Outline each uninfected red blood cell.
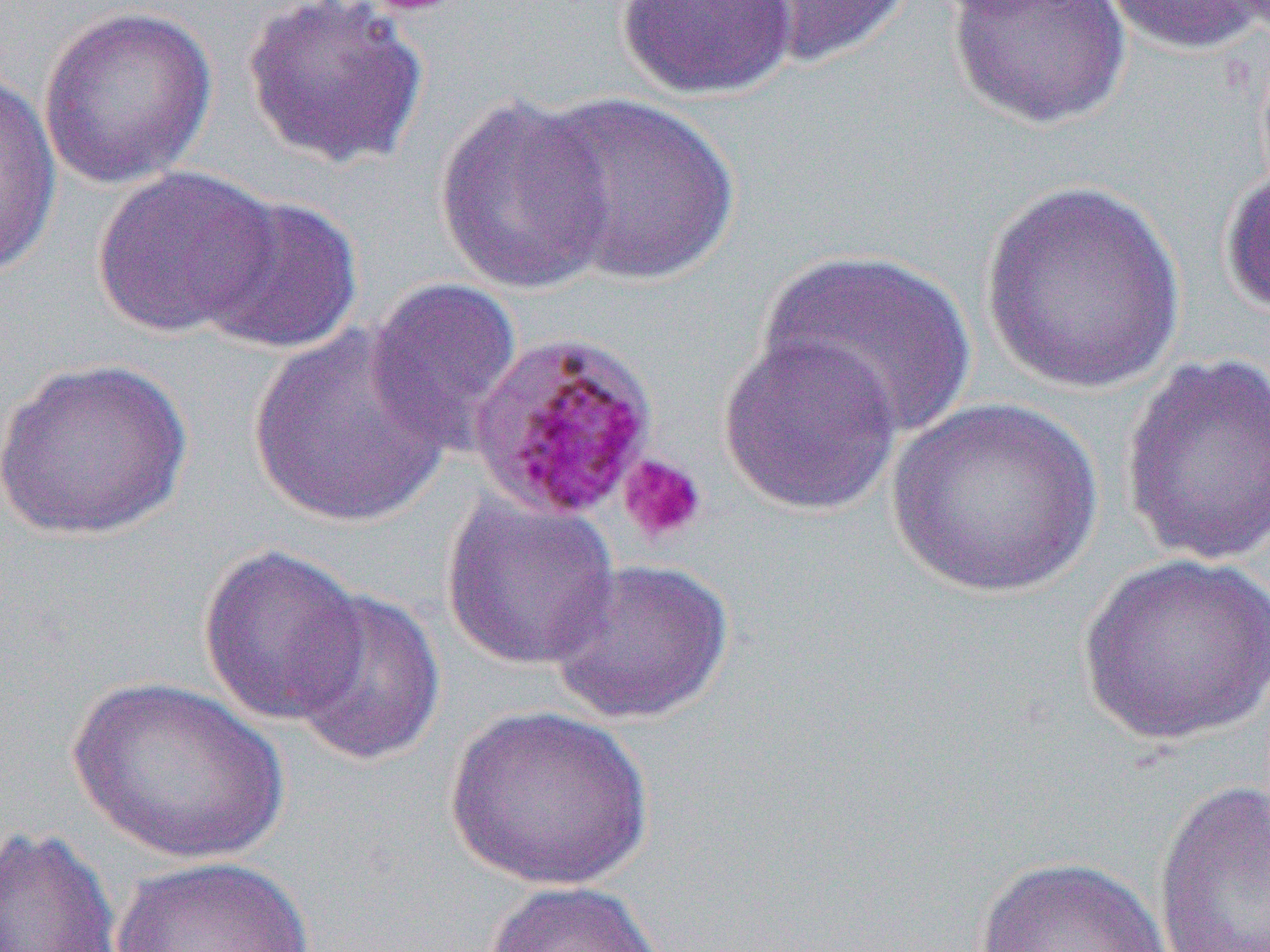

Approximate bounding boxes as (x1,y1)-(x2,y2) corner pairs in pixels.
Uninfected red blood cells: (240,0)-(430,172), (616,0)-(798,100), (734,0)-(916,70), (945,0)-(1133,131), (1099,0)-(1267,56), (37,4)-(218,189), (0,63)-(61,280), (532,92)-(742,287), (431,94)-(618,299), (91,165)-(278,338), (1220,167)-(1270,321), (978,179)-(1189,396), (194,194)-(364,357), (759,248)-(978,441), (363,278)-(524,455), (247,324)-(453,529), (716,332)-(904,517), (1119,352)-(1269,568), (0,357)-(194,541), (886,399)-(1104,600), (440,494)-(621,671), (197,543)-(368,727), (1076,551)-(1270,747), (546,557)-(736,726), (285,588)-(445,768), (68,676)-(290,865), (443,705)-(655,891), (1152,778)-(1270,950), (0,824)-(124,951), (973,855)-(1175,952), (110,856)-(318,952), (481,879)-(667,952).

slide-level diagnosis = Plasmodium malariae
modality = optical microscopy
platelet locations = approximate bounding boxes as (x1,y1)-(x2,y2) corner pairs in pixels: (617,453)-(708,545)
field of view = single
image size = 1270×952 pixels
magnification = 1000x
preparation = thin blood smear